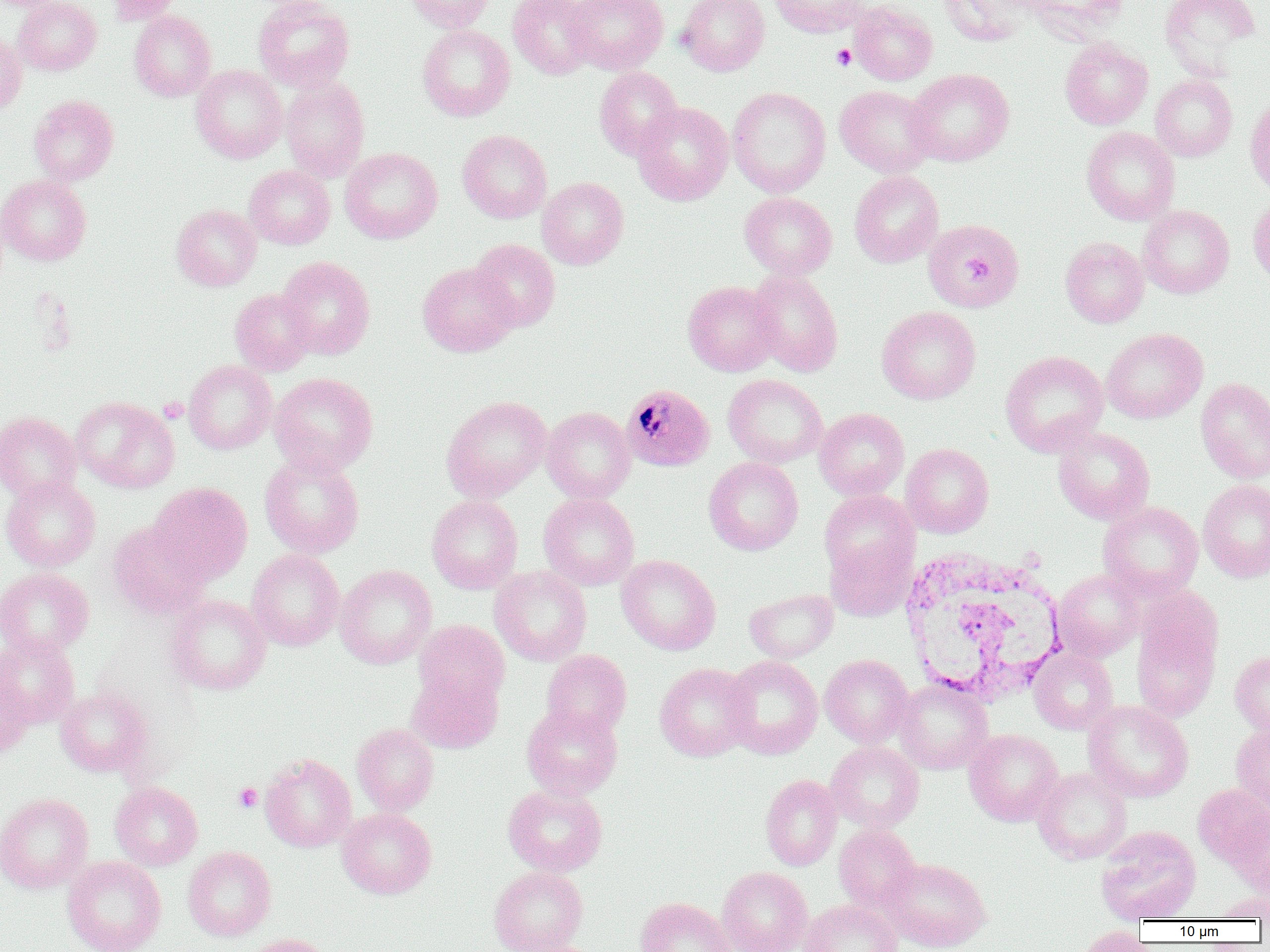

Approximate bounding boxes as [x1, y1, x2, y2] in pixels. Plasmodium malariae-infected red blood cell locations: [620, 383, 715, 472]. Platelet locations: [832, 44, 856, 71], [158, 397, 188, 423], [233, 782, 262, 812]. White blood cell locations: [899, 547, 1068, 705]. Uninfected red blood cell locations: [0, 0, 68, 11], [13, 0, 101, 75], [105, 0, 184, 25], [253, 0, 355, 92], [406, 0, 495, 32], [507, 0, 597, 79], [565, 0, 668, 74], [677, 0, 770, 76], [769, 0, 868, 38], [940, 0, 1033, 46], [1024, 0, 1128, 43], [1160, 0, 1261, 77], [849, 1, 937, 85], [129, 10, 216, 102], [417, 24, 515, 121], [0, 31, 26, 115], [1059, 38, 1153, 130], [191, 65, 287, 163], [594, 67, 683, 160], [905, 68, 1014, 166], [1151, 74, 1237, 161], [280, 77, 370, 179], [835, 85, 936, 177], [727, 87, 831, 197], [29, 95, 119, 185], [1245, 95, 1270, 195], [632, 102, 733, 206], [1081, 126, 1180, 225], [457, 130, 551, 223], [340, 147, 442, 244], [244, 165, 335, 249], [849, 170, 944, 268], [0, 175, 91, 265], [537, 177, 629, 269], [739, 192, 837, 280], [1248, 195, 1270, 286], [171, 204, 261, 291], [1138, 205, 1234, 298], [923, 218, 1024, 313], [1060, 237, 1149, 328], [468, 239, 560, 332], [277, 256, 375, 359], [417, 262, 520, 357], [747, 270, 843, 376], [683, 281, 782, 376], [230, 289, 316, 375], [877, 306, 981, 404], [1102, 328, 1208, 424], [1000, 350, 1109, 456], [184, 360, 277, 454], [269, 372, 378, 475], [723, 374, 828, 468], [1196, 378, 1270, 484], [441, 395, 552, 502], [72, 397, 179, 493], [542, 406, 635, 504], [814, 408, 909, 500], [0, 411, 82, 502], [1052, 427, 1154, 525], [901, 443, 994, 538], [259, 451, 364, 558], [704, 457, 803, 555], [1, 476, 100, 572], [1198, 479, 1270, 583], [149, 482, 252, 584], [820, 491, 917, 581], [538, 493, 640, 590], [426, 495, 523, 593], [1098, 501, 1203, 600], [107, 520, 212, 619], [826, 538, 915, 621], [247, 548, 345, 651], [616, 555, 721, 655], [335, 565, 436, 669], [490, 566, 591, 666], [0, 568, 93, 658], [1053, 569, 1144, 661], [745, 588, 838, 664], [166, 594, 271, 694], [1130, 600, 1223, 722], [413, 620, 509, 710], [0, 635, 80, 729], [1028, 648, 1118, 734], [541, 649, 632, 739], [1230, 650, 1270, 738], [1, 653, 33, 761], [819, 654, 914, 748], [722, 655, 822, 759], [655, 663, 756, 761], [407, 670, 503, 753], [894, 678, 993, 773], [55, 688, 153, 777], [1084, 700, 1194, 802], [522, 703, 623, 799], [352, 723, 439, 815], [1231, 724, 1270, 815], [964, 729, 1063, 826], [825, 741, 924, 832], [260, 753, 356, 852], [1033, 768, 1132, 864], [761, 774, 842, 870], [110, 781, 203, 871], [503, 783, 607, 876], [1193, 783, 1270, 872], [0, 792, 93, 893], [1233, 806, 1270, 897], [336, 807, 437, 899], [834, 824, 920, 911], [1096, 826, 1201, 923], [182, 846, 277, 941], [62, 856, 166, 952], [880, 857, 992, 952], [489, 865, 588, 952], [718, 866, 812, 952], [1210, 891, 1270, 921], [635, 897, 734, 952], [800, 899, 902, 952], [1074, 925, 1155, 952], [241, 933, 336, 952], [502, 938, 605, 952]. Slide-level diagnosis: Plasmodium malariae. Single field of view. Light microscopy. Captured at 1000x magnification. Image is 1270×952 pixels. Thin blood film.